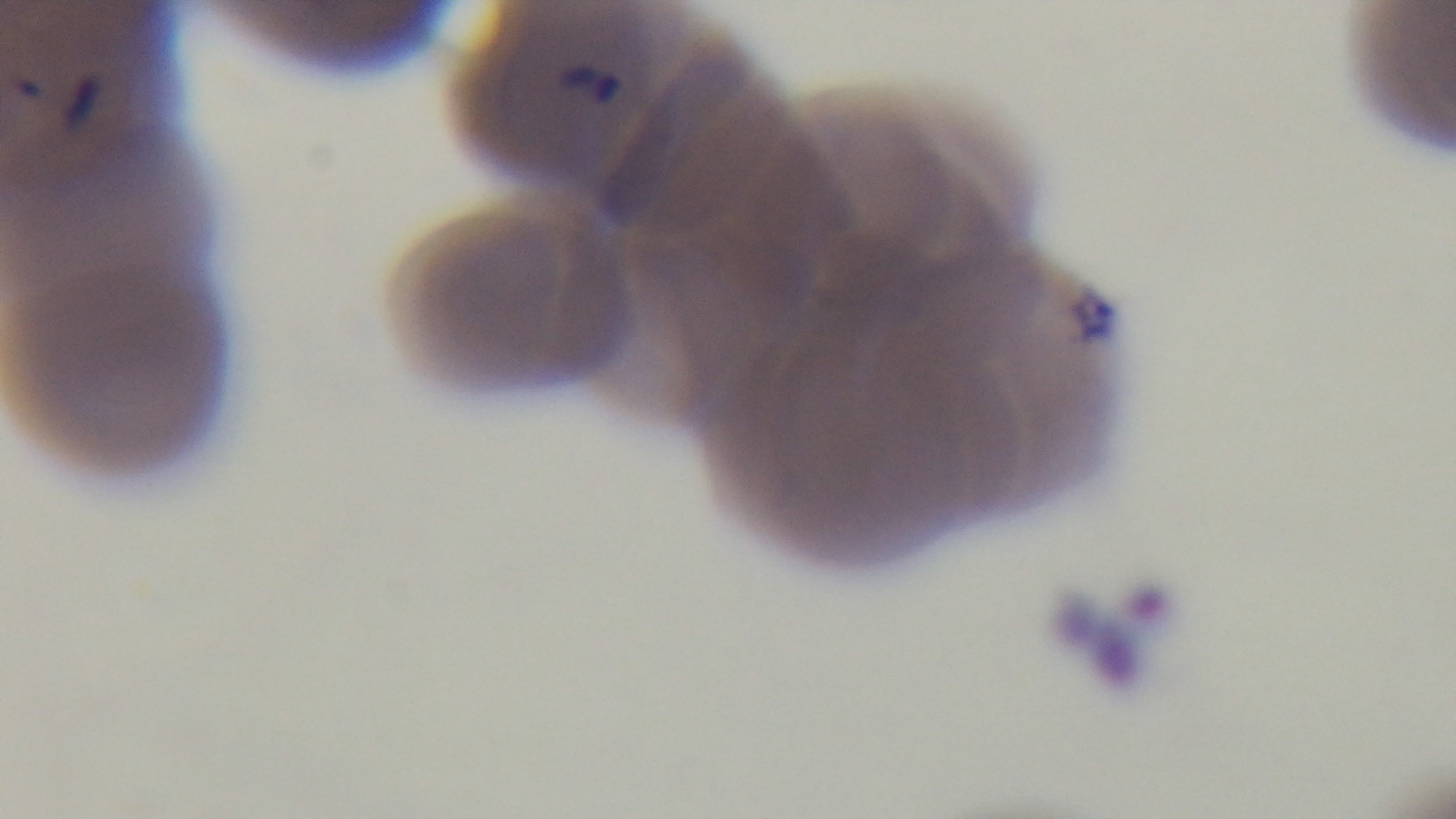
Oil-immersion objective, 100x. Preparation: thin. Malaria status: infected. One field from the slide. Captured with a mounted 4K digital camera. Giemsa-stained. Photomicrograph.